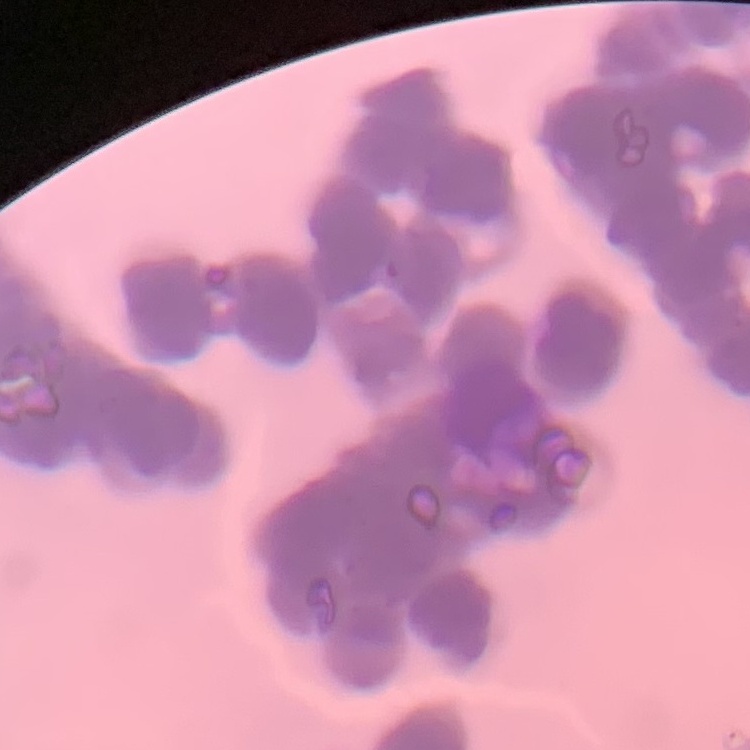
Summary:
  - Red blood cell morphology: rouleaux formation
  - Image type: one tile cut from a larger photomicrograph
  - Preparation: thin blood smear
  - Stain: Field's or Giemsa